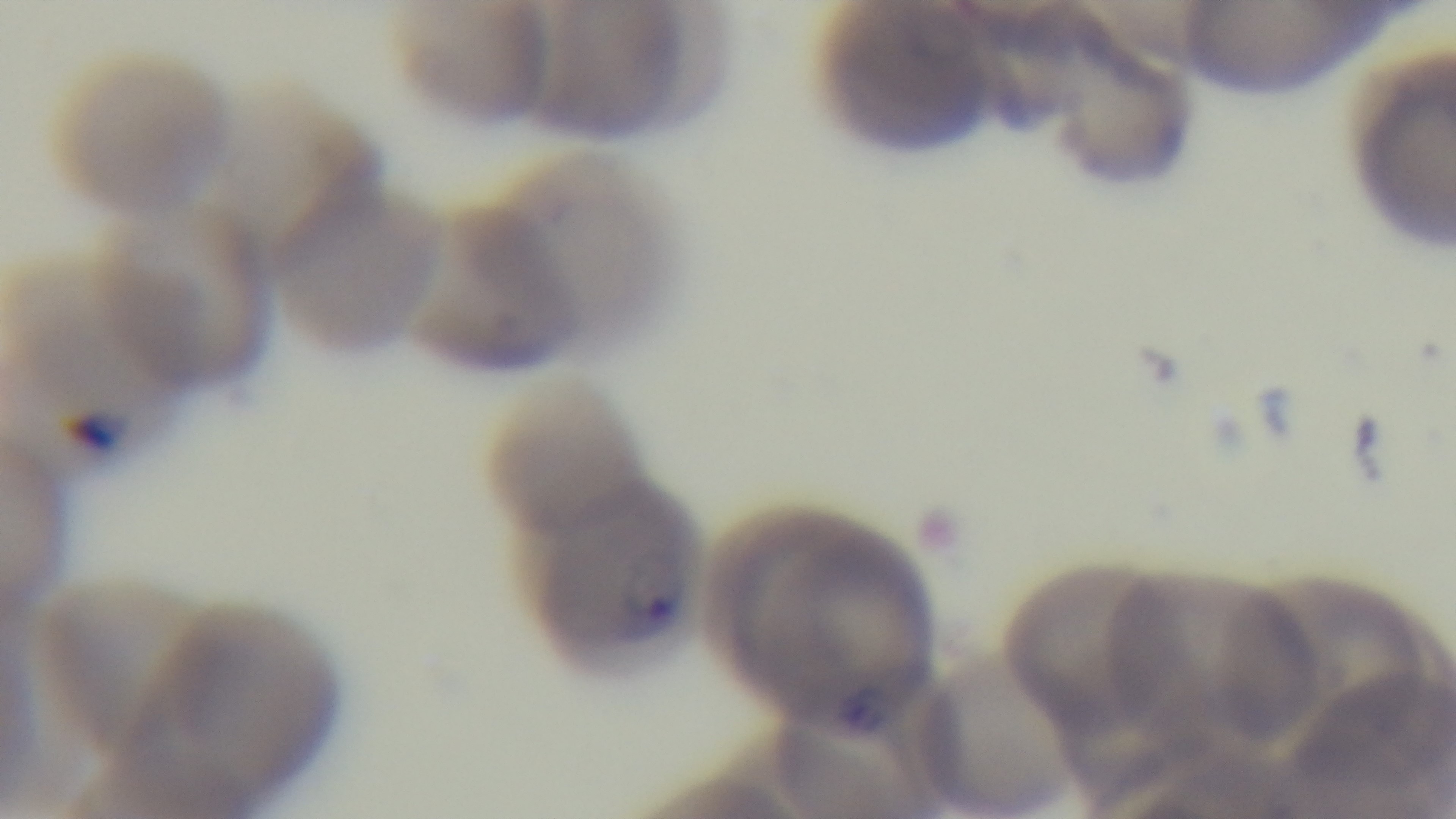
Oil-immersion objective, 100x. Captured with a mounted 4K digital camera. One field from the slide. Giemsa-stained. Photomicrograph. Malaria status: positive. Preparation: thin smear.